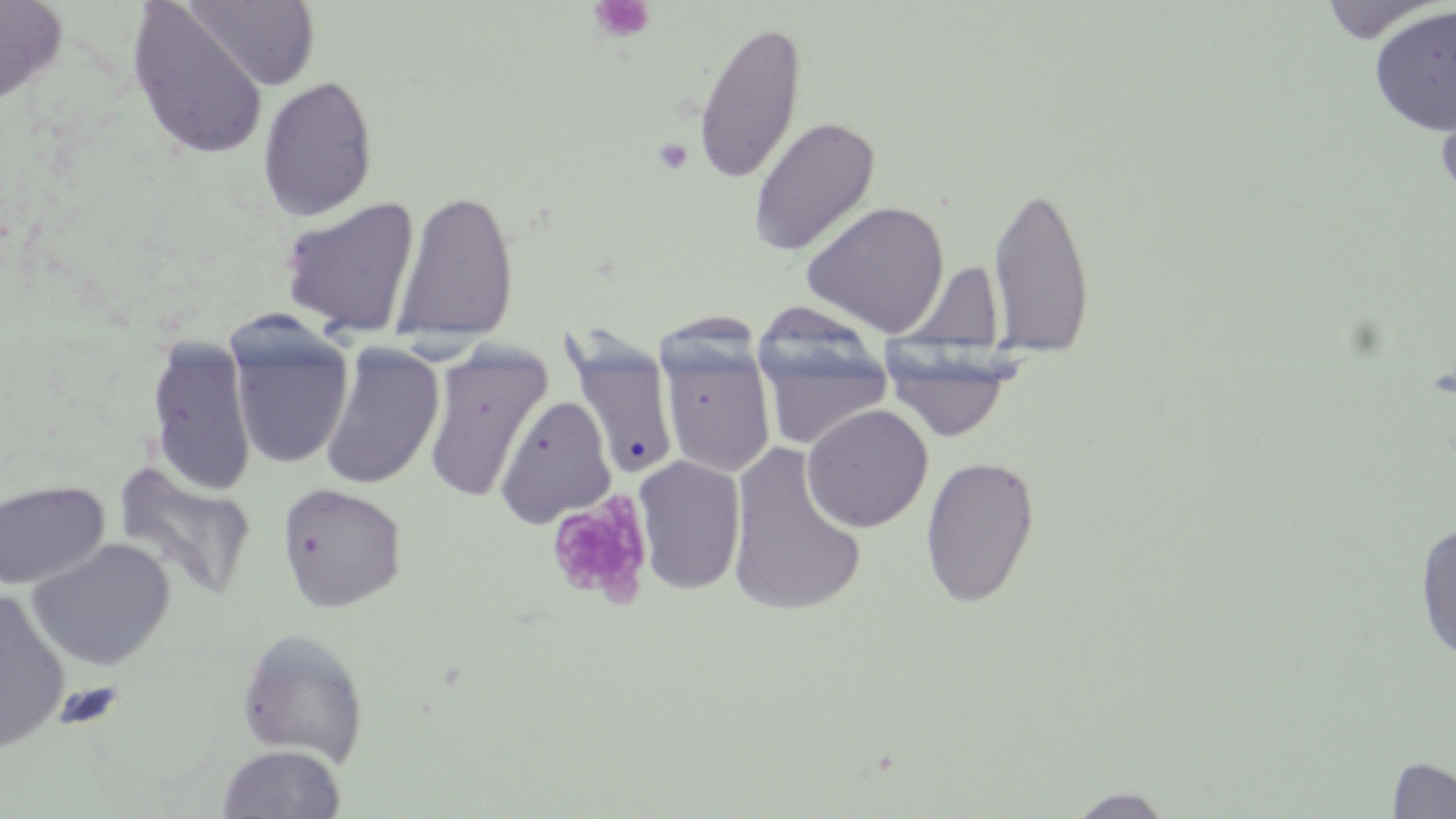
slide-level diagnosis = no evidence of blood parasites
uninfected red blood cell locations = approximate bounding boxes as named x1/y1/x2/y2 corners in pixels: (x1=0, y1=0, x2=67, y2=106), (x1=1317, y1=0, x2=1444, y2=44), (x1=185, y1=1, x2=320, y2=92), (x1=127, y1=3, x2=269, y2=161), (x1=1368, y1=5, x2=1456, y2=136), (x1=692, y1=19, x2=808, y2=186), (x1=257, y1=75, x2=378, y2=222), (x1=1435, y1=84, x2=1456, y2=211), (x1=748, y1=116, x2=881, y2=256), (x1=988, y1=181, x2=1096, y2=359), (x1=391, y1=188, x2=520, y2=347), (x1=278, y1=196, x2=421, y2=338), (x1=801, y1=200, x2=950, y2=337), (x1=752, y1=317, x2=896, y2=454), (x1=228, y1=323, x2=355, y2=470), (x1=146, y1=338, x2=257, y2=497), (x1=658, y1=338, x2=776, y2=478), (x1=568, y1=340, x2=679, y2=481), (x1=319, y1=342, x2=445, y2=492), (x1=422, y1=343, x2=551, y2=504), (x1=881, y1=343, x2=1022, y2=445), (x1=495, y1=395, x2=616, y2=528), (x1=801, y1=404, x2=933, y2=533), (x1=725, y1=442, x2=866, y2=618), (x1=633, y1=455, x2=746, y2=595), (x1=920, y1=455, x2=1040, y2=609), (x1=112, y1=461, x2=257, y2=600), (x1=0, y1=480, x2=109, y2=590), (x1=277, y1=482, x2=407, y2=613), (x1=1413, y1=521, x2=1456, y2=666), (x1=27, y1=538, x2=176, y2=671), (x1=0, y1=589, x2=70, y2=753), (x1=236, y1=628, x2=370, y2=767), (x1=215, y1=743, x2=347, y2=819), (x1=1386, y1=756, x2=1456, y2=817), (x1=1065, y1=787, x2=1177, y2=818)
magnification = 1000x
preparation = thin blood film
modality = light microscopy
image size = 1456×819 pixels
platelet locations = approximate bounding boxes as named x1/y1/x2/y2 corners in pixels: (x1=590, y1=0, x2=655, y2=42), (x1=654, y1=137, x2=693, y2=175), (x1=544, y1=493, x2=654, y2=608), (x1=54, y1=681, x2=126, y2=732)
stain = May-Grünwald-Giemsa
field of view = single